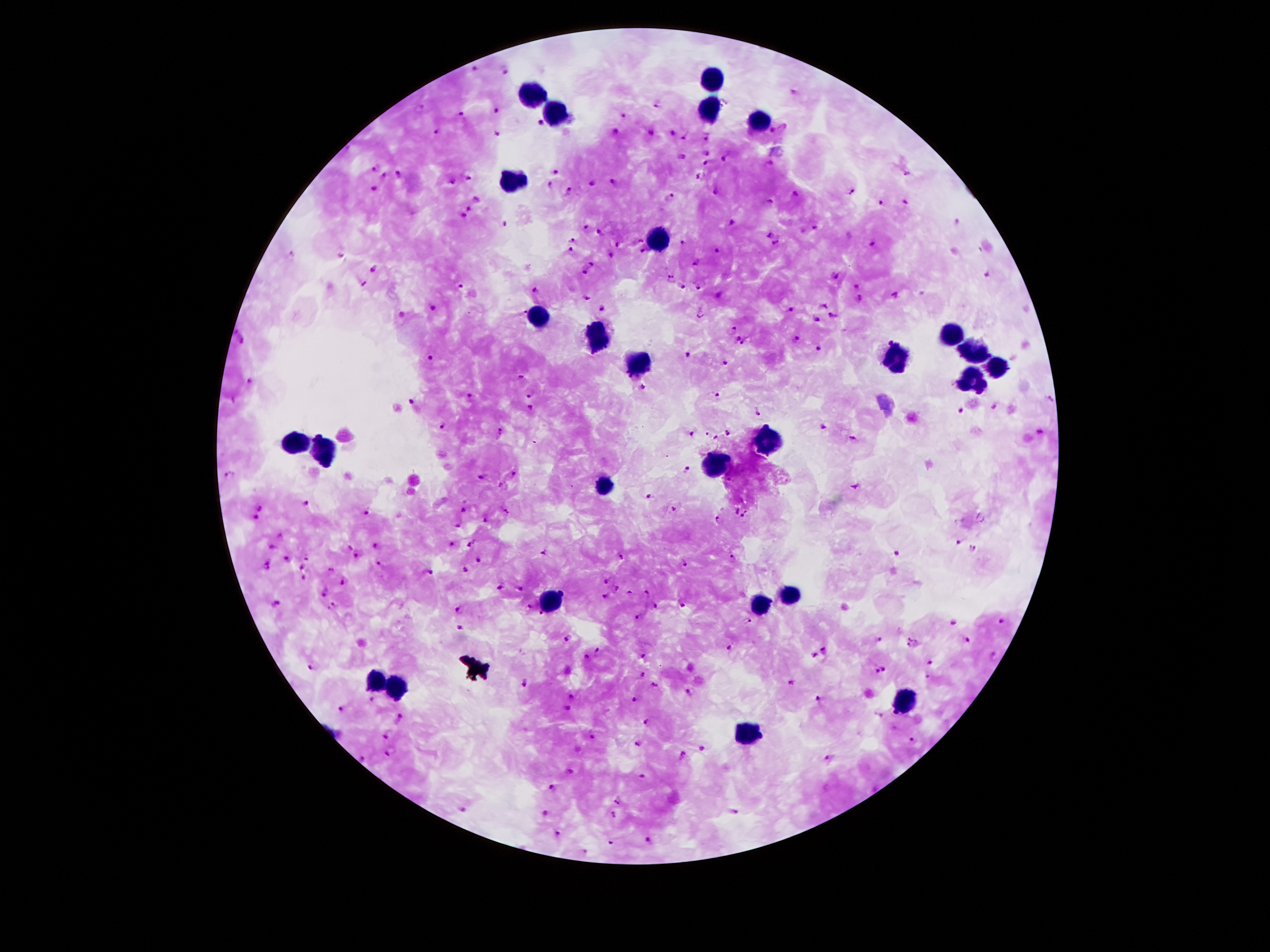
Approximate centers as {x, y} in pixels.
Summary:
  - Leukocyte locations: {713, 81}, {532, 97}, {554, 115}, {710, 117}, {754, 123}, {507, 182}, {658, 239}, {539, 320}, {948, 335}, {596, 336}, {972, 355}, {893, 359}, {636, 364}, {997, 368}, {970, 384}, {298, 443}, {769, 444}, {327, 452}, {718, 462}, {608, 486}, {791, 596}, {549, 604}, {764, 605}, {377, 683}, {399, 686}, {903, 701}, {751, 732}
  - Plasmodium parasite locations: {474, 70}, {508, 71}, {792, 94}, {658, 106}, {421, 108}, {496, 111}, {461, 115}, {622, 116}, {540, 124}, {778, 129}, {615, 130}, {438, 132}, {651, 132}, {496, 133}, {672, 134}, {707, 138}, {684, 139}, {706, 150}, {683, 156}, {727, 158}, {708, 161}, {769, 165}, {375, 169}, {907, 172}, {557, 173}, {399, 174}, {383, 176}, {470, 176}, {701, 177}, {451, 182}, {614, 183}, {592, 184}, {551, 185}, {374, 189}, {569, 192}, {717, 192}, {851, 192}, {795, 196}, {669, 197}, {475, 199}, {768, 202}, {881, 203}, {905, 204}, {468, 210}, {462, 218}, {733, 223}, {955, 223}, {504, 224}, {587, 227}, {814, 229}, {599, 234}, {769, 235}, {573, 240}, {641, 240}, {684, 242}, {776, 244}, {871, 244}, {619, 245}, {570, 251}, {641, 251}, {716, 251}, {290, 253}, {341, 254}, {611, 254}, {696, 263}, {589, 264}, {373, 269}, {585, 273}, {985, 275}, {835, 276}, {669, 278}, {364, 283}, {460, 285}, {683, 286}, {698, 286}, {855, 288}, {538, 292}, {718, 297}, {896, 297}, {587, 298}, {858, 299}, {822, 304}, {601, 307}, {432, 309}, {791, 310}, {833, 314}, {700, 315}, {815, 320}, {734, 329}, {737, 340}, {795, 340}, {242, 341}, {745, 344}, {818, 350}, {687, 354}, {431, 358}, {725, 364}, {522, 377}, {249, 382}, {641, 389}, {718, 394}, {527, 395}, {472, 397}, {410, 400}, {1050, 400}, {530, 409}, {961, 411}, {756, 412}, {823, 426}, {442, 428}, {499, 433}, {691, 433}, {727, 433}, {1040, 433}, {706, 434}, {714, 438}, {853, 439}, {687, 471}, {513, 474}, {229, 476}, {480, 477}, {855, 486}, {649, 496}, {307, 504}, {260, 509}, {464, 509}, {675, 509}, {736, 511}, {364, 512}, {507, 512}, {746, 516}, {253, 519}, {717, 519}, {485, 522}, {457, 527}, {280, 534}, {957, 542}, {452, 545}, {469, 545}, {375, 546}, {273, 547}, {349, 548}, {972, 549}, {543, 552}, {898, 554}, {355, 556}, {621, 556}, {285, 558}, {733, 559}, {306, 560}, {479, 562}, {380, 563}, {685, 564}, {268, 565}, {299, 568}, {330, 570}, {464, 571}, {429, 573}, {304, 579}, {343, 582}, {605, 582}, {500, 587}, {617, 588}, {519, 589}, {630, 593}, {324, 594}, {647, 594}, {606, 596}, {278, 602}, {684, 605}, {332, 606}, {657, 606}, {528, 607}, {458, 609}, {640, 615}, {541, 616}, {748, 620}, {1001, 621}, {953, 622}, {459, 628}, {912, 637}, {569, 640}, {879, 640}, {966, 641}, {729, 648}, {909, 648}, {825, 650}, {599, 651}, {994, 655}, {643, 656}, {814, 656}, {587, 658}, {930, 662}, {313, 667}, {885, 670}, {877, 671}, {642, 674}, {928, 677}, {523, 683}, {791, 683}, {654, 685}, {689, 694}, {569, 698}, {634, 698}, {818, 699}, {373, 701}, {342, 709}, {568, 709}, {400, 720}, {647, 721}, {388, 735}, {592, 738}, {912, 741}, {638, 743}, {702, 749}, {389, 752}, {682, 756}, {830, 759}, {364, 760}, {570, 773}, {643, 775}, {552, 789}, {617, 800}, {462, 811}, {735, 813}, {544, 814}, {614, 814}, {557, 835}, {648, 840}, {609, 842}, {583, 850}
  - Stain: Giemsa
  - Capture: smartphone through the microscope eyepiece
  - Patient malaria status: positive for Plasmodium falciparum
  - Preparation: thick blood smear
  - Magnification: 100x
  - Image size: 1270×952 pixels
  - Field of view: single